Name the parasite shown.
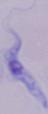

This is a trypanosome.

Photomicrograph. 1000x magnification.